State which parasite is depicted.
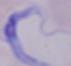
A trypanosome.

1000x magnification. Photomicrograph.